Outline each blood parasite and name the species.
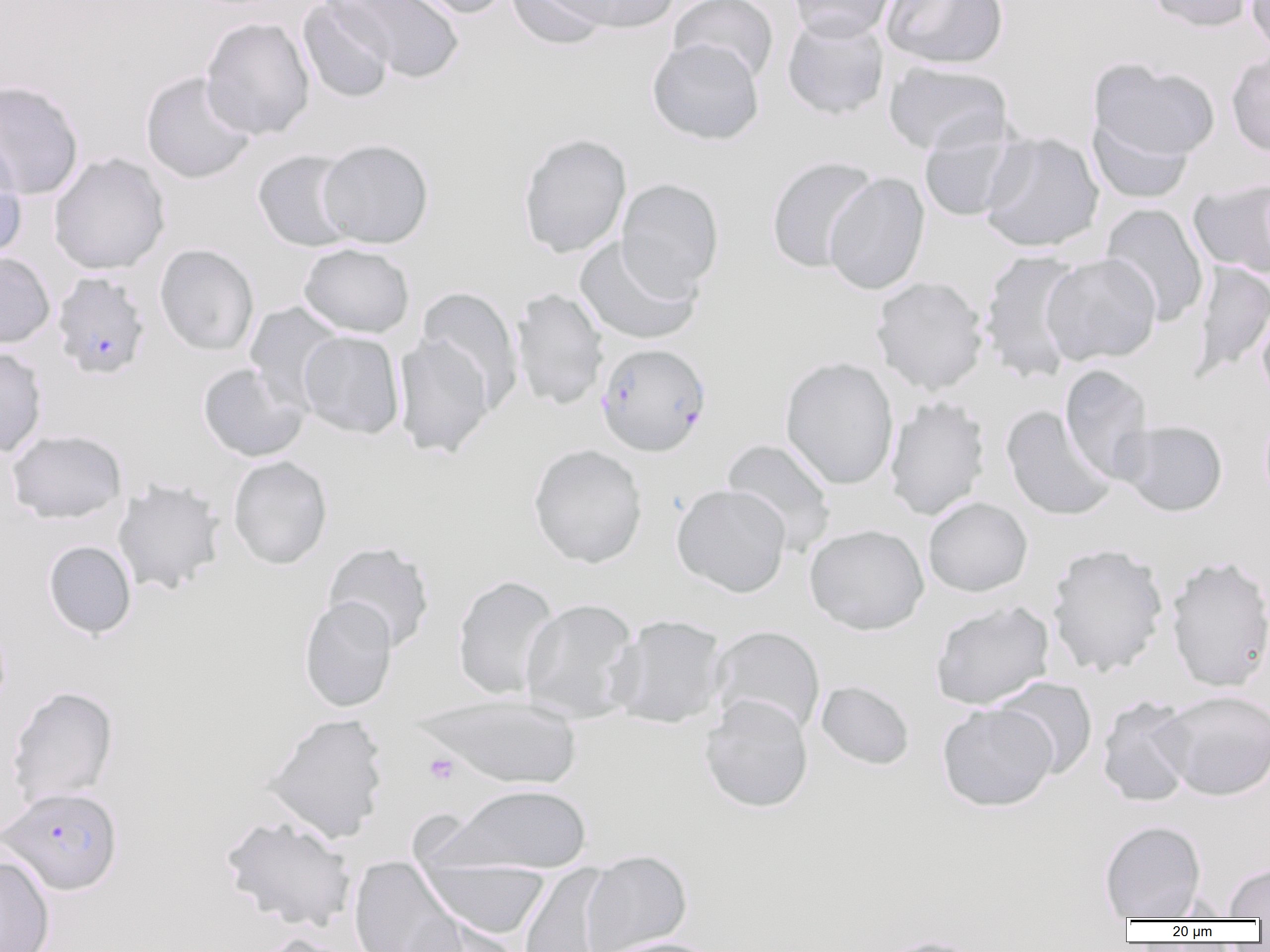
Approximate bounding boxes as (x1, y1, x2, y2) in pixels.
Plasmodium falciparum-infected red blood cells: (51, 272, 151, 379), (595, 342, 711, 456), (1, 787, 123, 895).
No Plasmodium ovale, Plasmodium malariae, Plasmodium vivax, Babesia divergens, or Trypanosoma brucei observed.

{
  "slide_level_diagnosis": "Plasmodium falciparum",
  "field_of_view": "one of a larger specimen",
  "image_size": "1270×952 pixels",
  "platelet_locations": "approximate bounding boxes as (x1, y1, x2, y2) in pixels: (424, 752, 459, 785)",
  "preparation": "thin blood smear",
  "modality": "optical microscopy",
  "uninfected_red_blood_cell_locations": "approximate bounding boxes as (x1, y1, x2, y2) in pixels: (298, 0, 396, 103), (332, 0, 465, 83), (399, 0, 513, 19), (506, 0, 610, 49), (550, 0, 679, 34), (669, 0, 780, 85), (786, 0, 898, 43), (881, 0, 1009, 70), (1146, 0, 1255, 33), (1246, 0, 1270, 60), (781, 13, 889, 120), (200, 17, 315, 140), (647, 38, 765, 146), (1226, 51, 1270, 157), (1088, 59, 1220, 166), (882, 61, 1013, 156), (140, 71, 257, 185), (0, 80, 84, 200), (1088, 114, 1194, 205), (917, 119, 1027, 222), (978, 131, 1105, 253), (518, 132, 632, 258), (317, 138, 434, 248), (0, 140, 27, 262), (252, 149, 359, 252), (48, 152, 170, 275), (766, 155, 880, 273), (823, 172, 930, 296), (616, 177, 725, 298), (1189, 178, 1270, 279), (1100, 203, 1210, 326), (573, 236, 703, 346), (298, 243, 416, 338), (155, 244, 260, 356), (977, 249, 1087, 384), (0, 251, 56, 349), (1041, 254, 1161, 366), (1190, 260, 1269, 381), (870, 276, 989, 395), (416, 286, 523, 413), (510, 287, 609, 412), (244, 302, 347, 410), (1256, 306, 1270, 409), (298, 331, 404, 439), (392, 334, 495, 459), (0, 346, 47, 458), (780, 356, 899, 489), (197, 362, 310, 462), (1059, 364, 1154, 484), (885, 396, 990, 521), (1000, 405, 1117, 522), (1118, 420, 1228, 517), (6, 429, 127, 524), (721, 438, 837, 555), (528, 443, 648, 568), (228, 456, 332, 569), (112, 478, 226, 596), (671, 483, 792, 597), (923, 497, 1033, 597), (804, 524, 929, 635), (43, 540, 137, 639), (322, 541, 435, 652), (1047, 542, 1168, 677), (1165, 555, 1270, 693), (452, 575, 560, 700), (298, 596, 397, 712), (520, 598, 640, 723), (930, 601, 1053, 710), (610, 614, 727, 729), (709, 625, 826, 737), (991, 676, 1098, 779), (815, 680, 915, 770), (6, 686, 119, 807), (1157, 690, 1270, 801), (419, 693, 583, 790), (699, 695, 814, 813), (1097, 695, 1197, 808), (937, 702, 1058, 812), (262, 713, 389, 843), (443, 783, 592, 873), (221, 815, 356, 931), (1099, 819, 1207, 920), (580, 849, 692, 952), (0, 854, 55, 952), (348, 856, 464, 952), (420, 859, 550, 939), (1223, 861, 1270, 919), (517, 864, 618, 952), (409, 915, 522, 952), (252, 932, 361, 952), (594, 936, 724, 952), (872, 936, 990, 952)",
  "magnification": "1000x"
}